Evaluate for malaria.
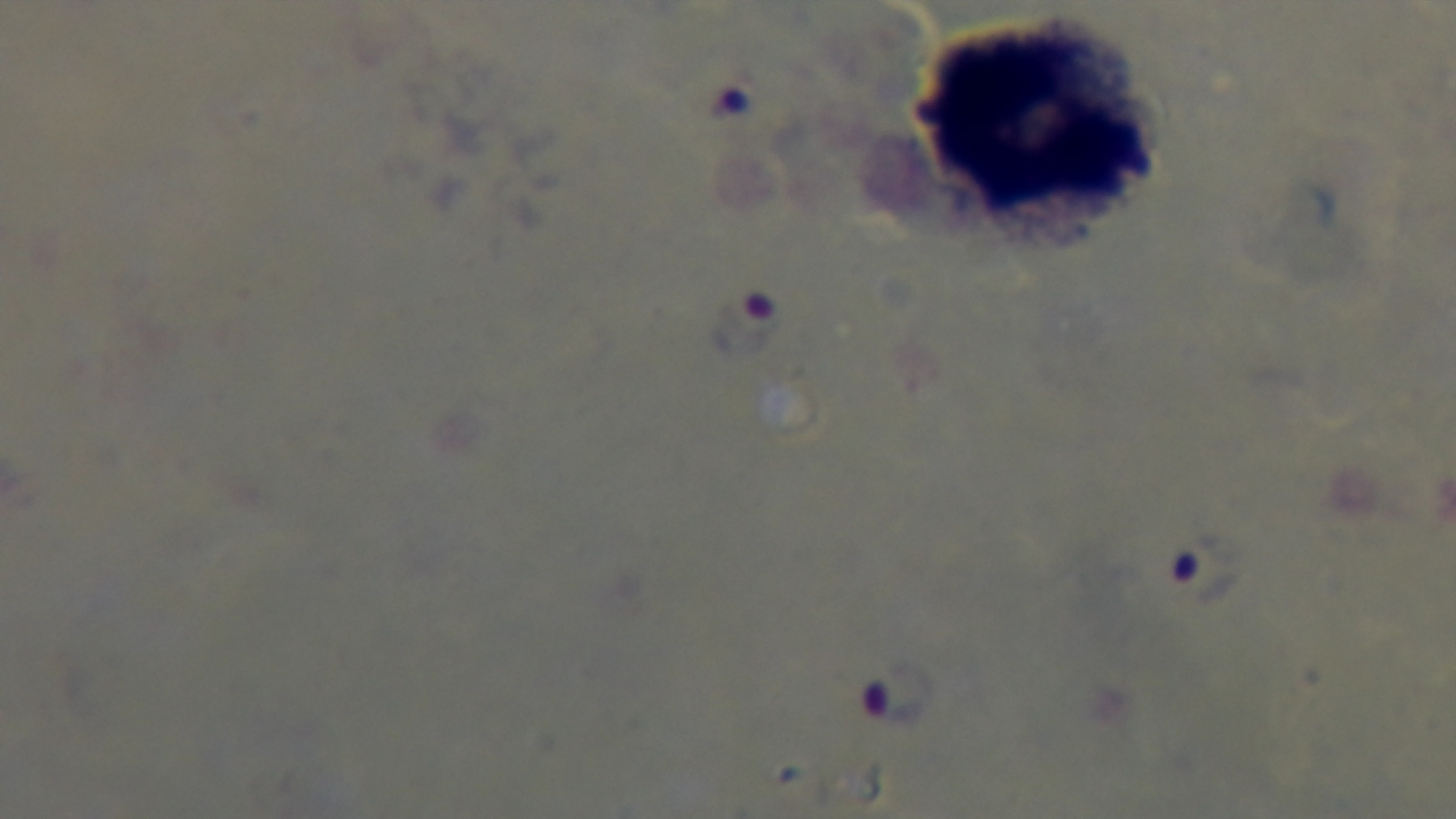
Infected.

Summary:
  - Objective: 100x oil immersion
  - Preparation: thick
  - Field of view: single
  - Stain: Giemsa
  - Modality: light microscopy
  - Capture: mounted 4K digital camera